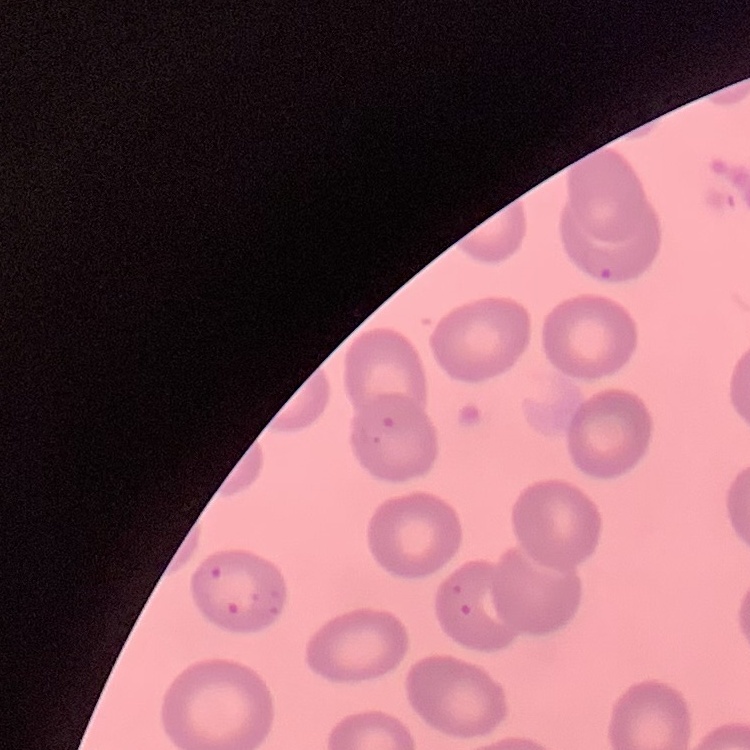

Summary:
  - Erythrocyte morphology: no rouleaux formation
  - Image type: square crop of a larger photomicrograph
  - Preparation: thin blood smear
  - Stain: Field's or Giemsa